Comment on the morphology of the erythrocytes.
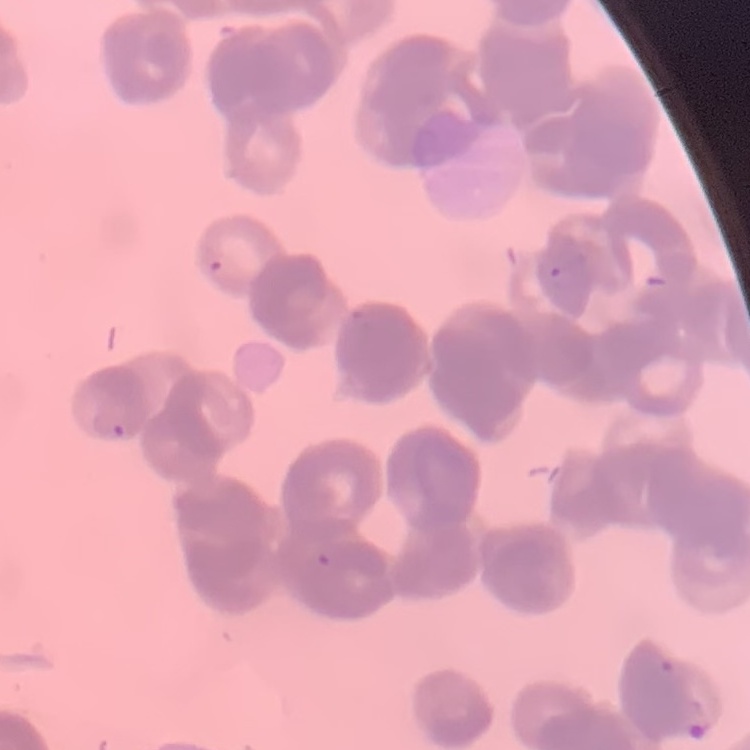
Rouleaux formation.

Field's or Giemsa stain. Thin blood smear. Square crop of a larger photomicrograph.